Locate every Plasmodium parasite.
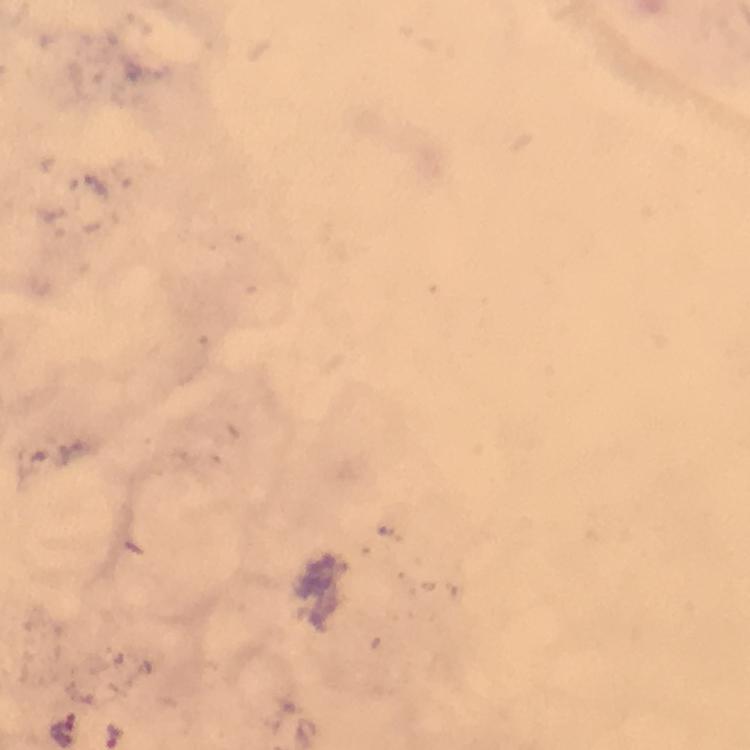
Approximate centers as {x, y} in pixels.
Plasmodium parasites: {66, 734}, {115, 736}.

context = from a diagnostic examination for malaria
stain = Giemsa
immersion oil = applied
preparation = thick blood film
magnification = 100x
capture = smartphone camera through the microscope
cropped from = a single field of view
image size = 750×750 pixels